Assess this cell for malaria.
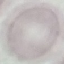

It is uninfected.

Summary:
  - Stain: Giemsa
  - Capture: smartphone camera at the microscope eyepiece
  - Image type: automatically extracted cell patch, resized to 64 × 64 pixels
  - Preparation: thin blood film